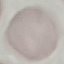

Result: negative for malaria parasites. Thin blood smear. Giemsa-stained preparation. Photographed with a smartphone camera at the microscope eyepiece. Cell patch, automatically extracted from a larger field of view and resized to 64 × 64 pixels.